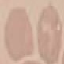

Summary:
  - Malaria status: uninfected
  - Image type: automatically extracted cell patch, resized to 64 × 64 pixels
  - Stain: Giemsa
  - Capture: smartphone through the microscope eyepiece
  - Preparation: thin blood smear